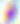
Summary:
  - Identification: Toxoplasma gondii
  - Modality: photomicrograph
  - Magnification: 400x